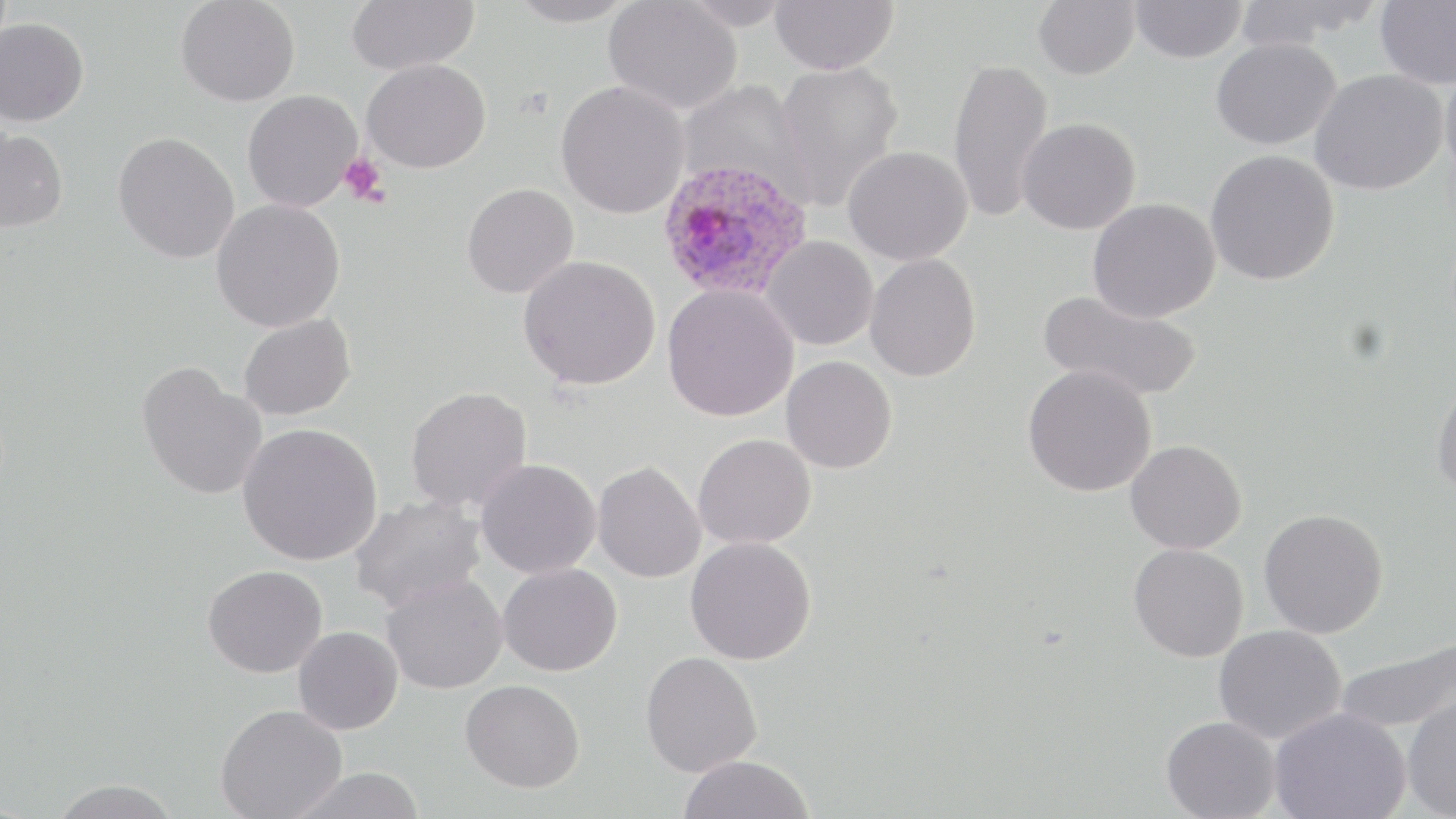

slide-level diagnosis = Plasmodium ovale
field of view = single
image size = 1456×819 pixels
modality = optical microscopy
uninfected red blood cell locations = approximate bounding boxes as [x1, y1, x2, y2] in pixels: [175, 0, 300, 107], [345, 0, 479, 75], [505, 0, 640, 28], [678, 0, 794, 30], [770, 0, 898, 75], [1033, 0, 1140, 80], [1130, 0, 1247, 64], [1375, 0, 1456, 89], [604, 1, 742, 114], [1231, 1, 1382, 49], [0, 17, 89, 126], [1210, 37, 1341, 150], [948, 57, 1055, 224], [362, 59, 490, 173], [772, 61, 904, 211], [1439, 61, 1456, 182], [1310, 69, 1447, 195], [677, 80, 810, 202], [555, 81, 690, 218], [242, 89, 363, 212], [1017, 117, 1141, 235], [0, 127, 68, 233], [113, 132, 240, 264], [843, 145, 973, 265], [1205, 149, 1340, 285], [461, 183, 578, 298], [1088, 198, 1220, 322], [211, 199, 346, 332], [761, 235, 878, 350], [865, 253, 981, 381], [518, 255, 660, 390], [662, 283, 799, 421], [1038, 290, 1201, 402], [239, 314, 356, 421], [781, 356, 897, 473], [137, 362, 267, 500], [1022, 363, 1157, 497], [1432, 378, 1456, 499], [405, 386, 533, 513], [237, 422, 383, 565], [693, 433, 817, 549], [1125, 439, 1247, 554], [475, 459, 602, 579], [592, 461, 707, 583], [349, 495, 486, 613], [1259, 508, 1389, 638], [685, 536, 816, 665], [1129, 543, 1249, 662], [498, 563, 622, 676], [203, 564, 328, 678], [381, 574, 507, 694], [1213, 625, 1347, 744], [293, 626, 403, 735], [1335, 635, 1455, 735], [640, 651, 763, 777], [460, 679, 585, 792], [1402, 691, 1456, 819], [215, 704, 347, 819], [1269, 707, 1410, 819], [1161, 715, 1280, 819], [678, 754, 814, 819], [286, 767, 428, 819], [45, 779, 185, 818]
preparation = thin blood film
platelet locations = approximate bounding boxes as [x1, y1, x2, y2] in pixels: [338, 151, 389, 207]
magnification = 1000x
Plasmodium ovale-infected red blood cell locations = approximate bounding boxes as [x1, y1, x2, y2] in pixels: [656, 158, 813, 301]
stain = May-Grünwald-Giemsa